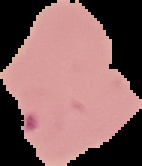

Summary:
  - Result: Plasmodium parasites identified
  - Preparation: thin blood smear
  - Image size: 142×166 pixels
  - Image type: segmented cell region on a black background